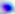

Micrograph. Toxoplasma gondii is seen. 400x magnification.